State which parasite is depicted.
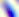
This is Toxoplasma gondii.

Summary:
  - Modality: photomicrograph
  - Magnification: 400x